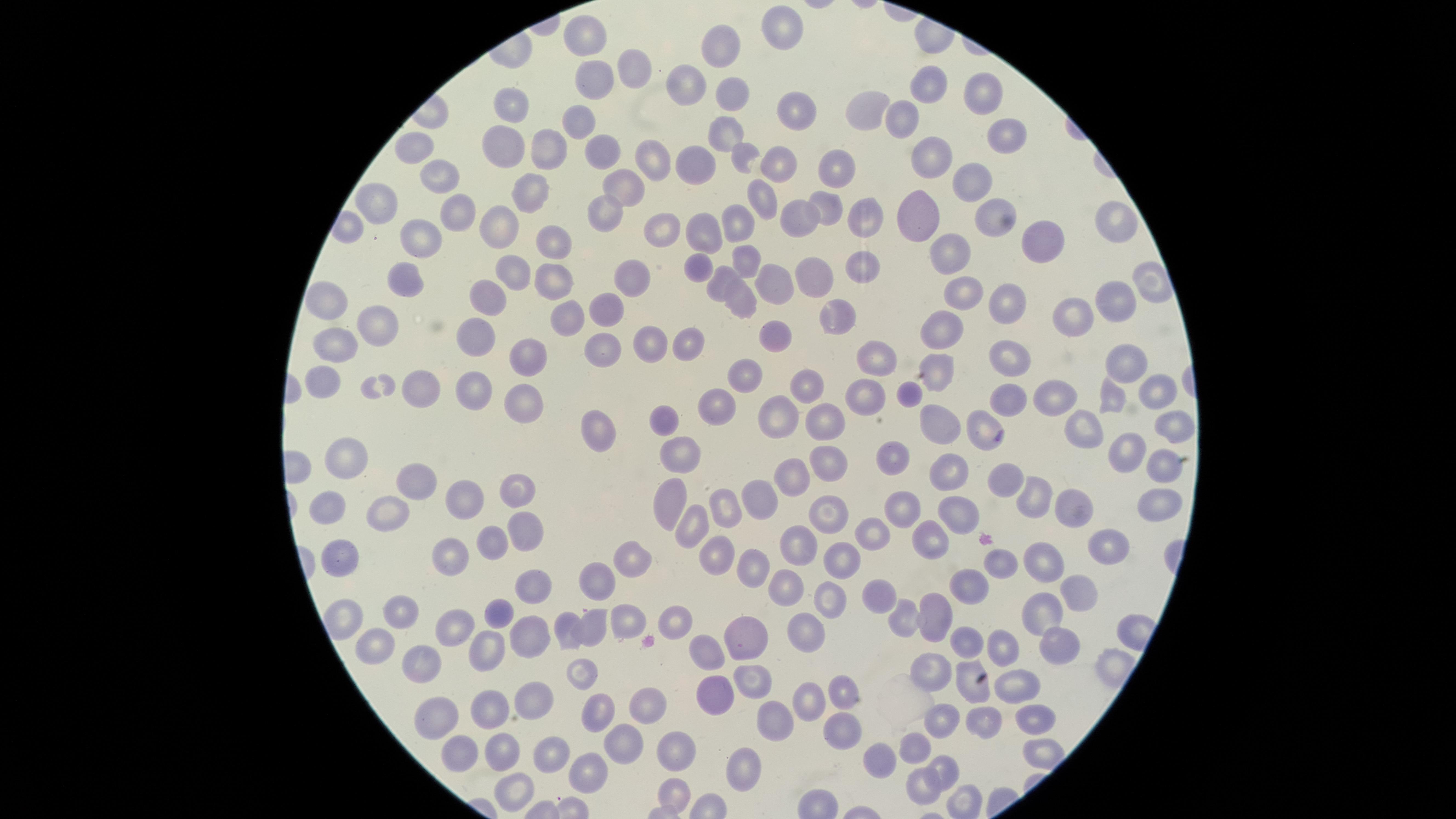

{
  "capture": "smartphone photograph through the microscope eyepiece",
  "preparation": "thin blood smear",
  "visible_region": "circular",
  "stain": "Giemsa",
  "uninfected_red_blood_cells": "approximate marker points as {x, y} in pixels: {787, 31}, {582, 33}, {720, 51}, {630, 74}, {590, 79}, {929, 85}, {687, 86}, {980, 93}, {730, 101}, {860, 103}, {513, 106}, {794, 109}, {900, 116}, {576, 119}, {721, 132}, {999, 140}, {547, 144}, {501, 145}, {417, 151}, {600, 153}, {933, 156}, {744, 159}, {773, 161}, {649, 166}, {832, 168}, {701, 172}, {441, 178}, {969, 179}, {625, 187}, {529, 191}, {761, 196}, {825, 209}, {606, 210}, {986, 210}, {382, 211}, {865, 213}, {912, 216}, {454, 218}, {797, 219}, {1113, 224}, {502, 227}, {741, 228}, {656, 233}, {704, 233}, {420, 237}, {1049, 238}, {553, 244}, {955, 248}, {746, 258}, {698, 260}, {854, 265}, {516, 273}, {811, 273}, {551, 279}, {402, 280}, {636, 280}, {721, 280}, {780, 284}, {958, 290}, {324, 299}, {490, 301}, {1012, 302}, {1115, 302}, {741, 303}, {608, 309}, {838, 311}, {1072, 317}, {559, 320}, {382, 322}, {941, 328}, {772, 333}, {692, 337}, {643, 339}, {476, 341}, {334, 342}, {600, 346}, {1006, 353}, {868, 354}, {940, 358}, {531, 359}, {1125, 361}, {745, 378}, {324, 382}, {809, 384}, {475, 389}, {859, 390}, {428, 391}, {1154, 391}, {1059, 392}, {907, 394}, {1003, 394}, {1115, 395}, {516, 403}, {713, 404}, {659, 415}, {785, 416}, {1170, 420}, {826, 422}, {941, 425}, {979, 425}, {1083, 427}, {596, 433}, {1129, 448}, {684, 449}, {346, 457}, {831, 464}, {891, 467}, {1161, 467}, {946, 472}, {785, 477}, {421, 481}, {1031, 490}, {520, 491}, {760, 495}, {465, 498}, {664, 502}, {1154, 502}, {723, 504}, {1079, 504}, {331, 508}, {826, 509}, {388, 510}, {902, 512}, {953, 518}, {691, 529}, {524, 530}, {871, 535}, {933, 537}, {494, 541}, {795, 543}, {712, 547}, {1103, 549}, {344, 550}, {453, 550}, {635, 561}, {840, 562}, {1036, 562}, {751, 565}, {1006, 565}, {598, 580}, {785, 584}, {969, 585}, {529, 588}, {1079, 588}, {876, 596}, {820, 599}, {398, 609}, {498, 613}, {909, 614}, {1042, 614}, {936, 615}, {625, 617}, {670, 622}, {565, 623}, {597, 625}, {452, 628}, {527, 628}, {800, 632}, {743, 636}, {961, 643}, {1057, 643}, {375, 644}, {1008, 645}, {490, 648}, {710, 652}, {423, 657}, {936, 659}, {586, 668}, {751, 671}, {962, 676}, {1014, 686}, {532, 691}, {714, 696}, {844, 696}, {814, 701}, {647, 704}, {598, 706}, {488, 712}, {441, 714}, {1035, 717}, {941, 719}, {776, 720}, {840, 723}, {981, 723}, {621, 741}, {916, 744}, {676, 749}, {501, 750}, {457, 753}, {879, 756}, {551, 757}, {744, 769}, {948, 769}, {590, 774}, {517, 786}, {919, 787}, {675, 789}, {958, 798}",
  "image_size": "1456×819 pixels",
  "field_of_view": "single",
  "presence": "no malaria parasites detected"
}